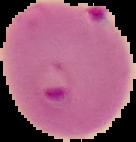
image_type: segmented cell region on a black background
malaria_status: parasitized
image_size: 136×142 pixels
preparation: thin blood smear